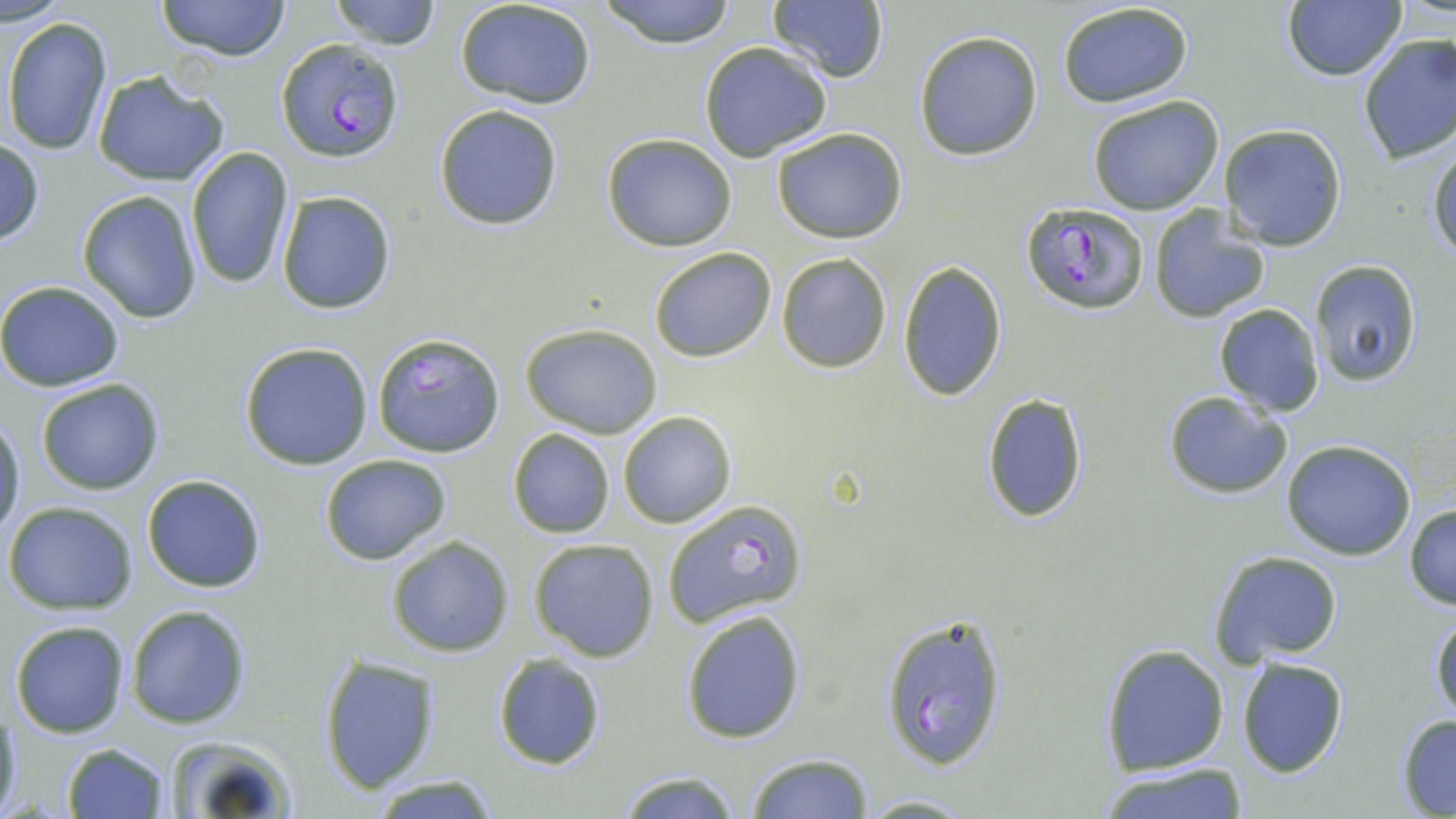

Approximate bounding boxes as (x1, y1, x2, y2) in pixels. Uninfected red blood cell locations: (155, 0, 293, 61), (328, 0, 442, 48), (597, 0, 740, 48), (767, 0, 890, 82), (1281, 1, 1406, 82), (457, 2, 597, 108), (1056, 2, 1198, 110), (3, 15, 114, 156), (913, 30, 1042, 160), (1356, 33, 1456, 165), (699, 42, 830, 162), (91, 67, 231, 188), (1085, 96, 1226, 215), (433, 104, 563, 231), (1219, 124, 1348, 251), (770, 126, 910, 243), (601, 132, 737, 251), (0, 138, 44, 246), (1428, 139, 1456, 262), (187, 147, 297, 290), (76, 190, 204, 324), (276, 192, 397, 314), (1147, 206, 1271, 322), (648, 248, 776, 362), (776, 253, 892, 373), (898, 260, 1008, 401), (1309, 261, 1424, 388), (0, 280, 124, 390), (1213, 303, 1324, 417), (520, 324, 663, 438), (372, 332, 505, 459), (237, 341, 374, 469), (34, 377, 166, 496), (1162, 391, 1293, 498), (981, 392, 1090, 525), (619, 412, 738, 528), (0, 413, 25, 543), (507, 427, 615, 538), (1281, 439, 1416, 560), (320, 455, 452, 564), (142, 474, 266, 594), (2, 501, 138, 614), (1404, 503, 1456, 611), (386, 535, 516, 658), (528, 537, 660, 662), (1207, 549, 1344, 666), (125, 603, 254, 730), (679, 607, 808, 745), (1430, 611, 1456, 725), (10, 619, 131, 738), (1098, 642, 1230, 776), (491, 653, 608, 770), (317, 654, 442, 794), (1236, 655, 1350, 779), (1, 702, 22, 819), (1395, 712, 1456, 816), (159, 734, 300, 817), (61, 742, 171, 818), (747, 753, 873, 819), (1096, 764, 1251, 819), (612, 770, 741, 818), (369, 773, 502, 817), (858, 793, 982, 817). Plasmodium falciparum-infected red blood cell locations: (276, 40, 404, 162), (1020, 200, 1148, 314), (662, 495, 806, 627), (880, 612, 1010, 773). Slide-level diagnosis: Plasmodium falciparum. One field of a larger specimen. Light microscopy. Captured at 1000x magnification. Thin blood film. May-Grünwald-Giemsa-stained preparation. Image is 1456×819 pixels.